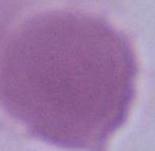

Summary:
  - Modality: photomicrograph
  - Magnification: 1000x
  - Identification: red blood cell